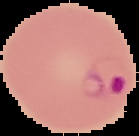
Summary:
  - Malaria status: parasitized
  - Preparation: thin blood smear
  - Image size: 139×136 pixels
  - Image type: cell region segmented out of the field of view; surrounding area masked to black